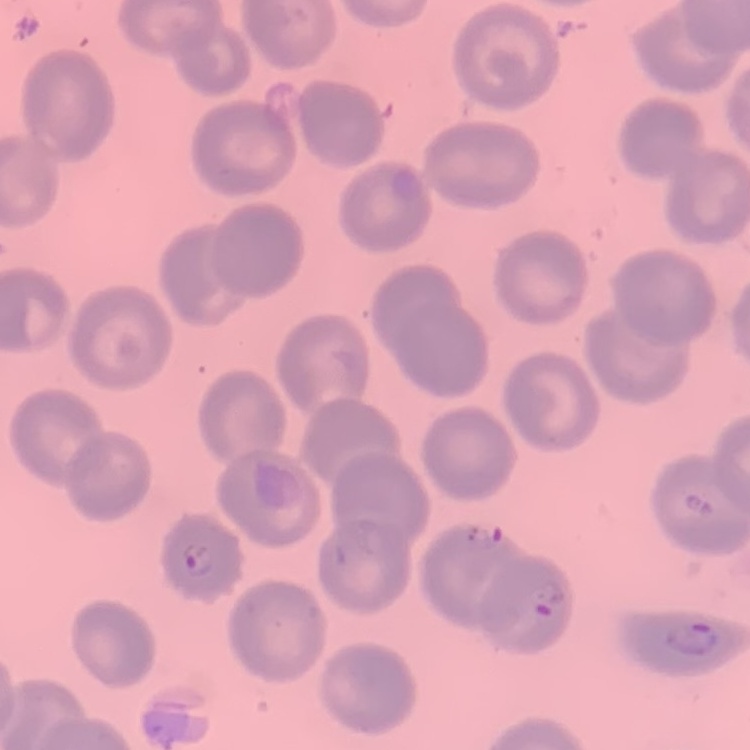

The erythrocytes exhibit no rouleaux formation. One tile cut from a larger photomicrograph. Thin blood smear. Stained with either Field's or Giemsa.